Classify this cell by malaria status.
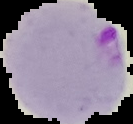
It is parasitized.

preparation: thin blood film
image_type: segmented cell region on a black background
image_size: 133×124 pixels